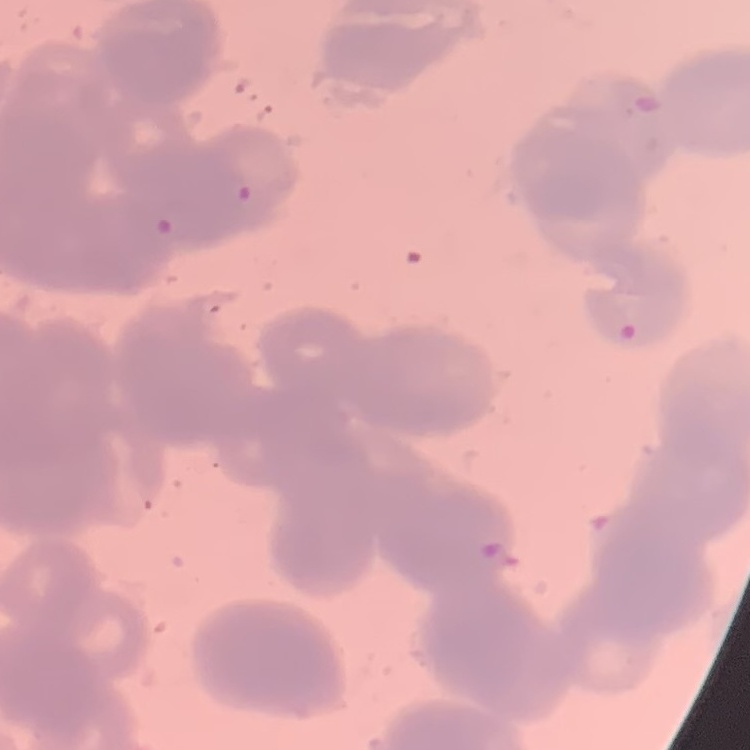
The red blood cells exhibit rouleaux formation. Thin blood smear. Square crop of a larger photomicrograph. Field's or Giemsa stain.